Outline each uninfected red blood cell.
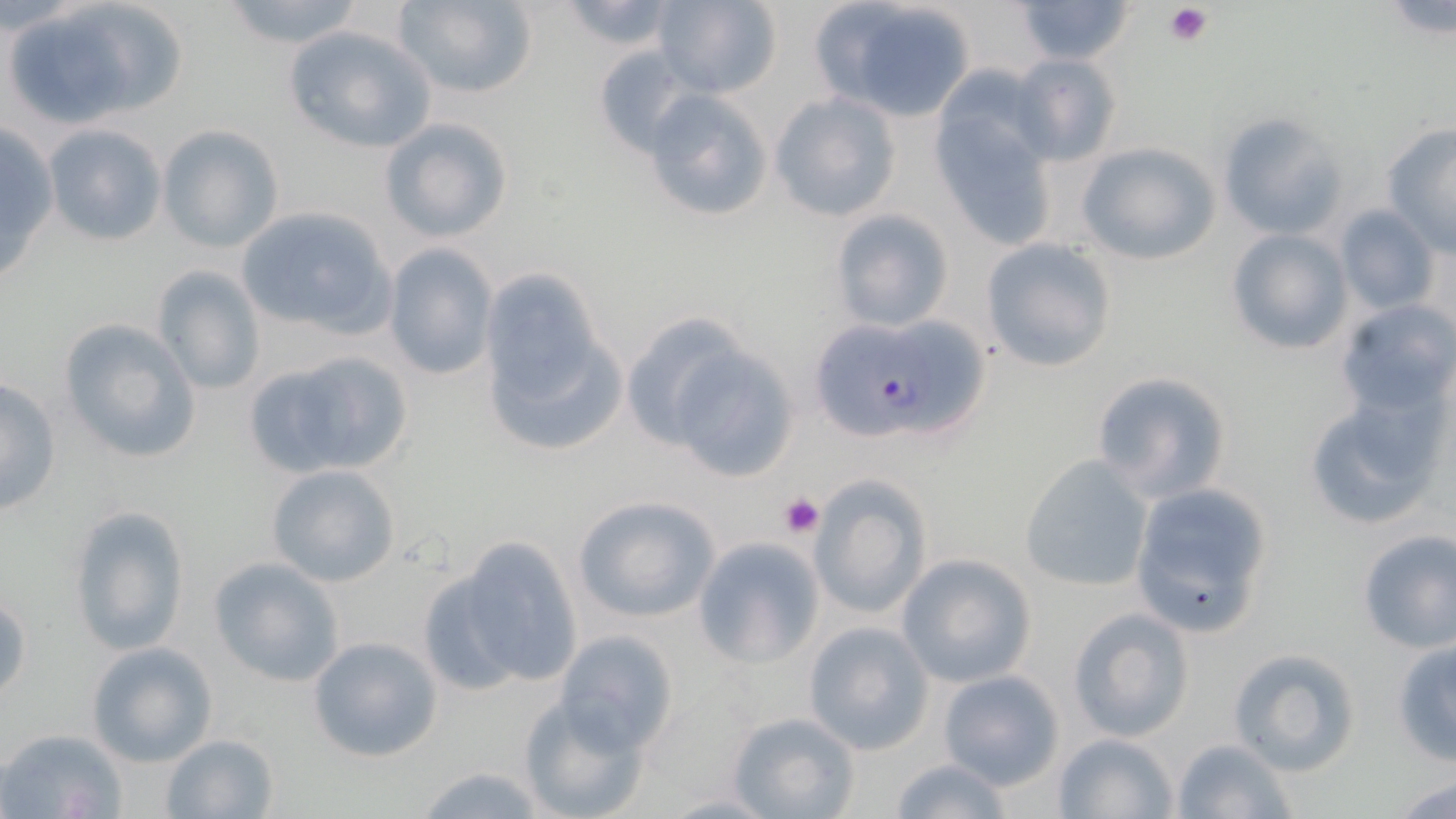

Approximate bounding boxes as named x1/y1/x2/y2 corners in pixels.
Uninfected red blood cells: (x1=12, y1=0, x2=186, y2=127), (x1=214, y1=0, x2=370, y2=49), (x1=393, y1=0, x2=538, y2=98), (x1=651, y1=0, x2=783, y2=97), (x1=809, y1=0, x2=981, y2=119), (x1=1016, y1=0, x2=1132, y2=64), (x1=556, y1=1, x2=682, y2=51), (x1=282, y1=23, x2=437, y2=154), (x1=591, y1=45, x2=699, y2=156), (x1=1011, y1=54, x2=1123, y2=167), (x1=642, y1=88, x2=774, y2=222), (x1=769, y1=91, x2=902, y2=222), (x1=931, y1=103, x2=1058, y2=252), (x1=1217, y1=112, x2=1349, y2=239), (x1=379, y1=115, x2=514, y2=243), (x1=0, y1=122, x2=58, y2=286), (x1=41, y1=124, x2=168, y2=247), (x1=156, y1=125, x2=284, y2=253), (x1=1380, y1=125, x2=1455, y2=252), (x1=1075, y1=140, x2=1220, y2=265), (x1=234, y1=205, x2=398, y2=342), (x1=1334, y1=206, x2=1440, y2=314), (x1=829, y1=208, x2=954, y2=332), (x1=1226, y1=229, x2=1352, y2=354), (x1=980, y1=237, x2=1118, y2=374), (x1=382, y1=243, x2=499, y2=381), (x1=153, y1=264, x2=267, y2=395), (x1=481, y1=276, x2=623, y2=455), (x1=1334, y1=300, x2=1456, y2=422), (x1=619, y1=310, x2=763, y2=455), (x1=59, y1=318, x2=201, y2=465), (x1=660, y1=340, x2=802, y2=483), (x1=244, y1=347, x2=414, y2=480), (x1=1090, y1=370, x2=1233, y2=503), (x1=1, y1=375, x2=63, y2=518), (x1=1303, y1=397, x2=1445, y2=530), (x1=1018, y1=453, x2=1153, y2=591), (x1=265, y1=464, x2=403, y2=588), (x1=803, y1=476, x2=932, y2=622), (x1=1128, y1=481, x2=1275, y2=639), (x1=571, y1=494, x2=721, y2=623), (x1=69, y1=503, x2=191, y2=659), (x1=1356, y1=529, x2=1456, y2=654), (x1=435, y1=534, x2=585, y2=695), (x1=692, y1=536, x2=825, y2=668), (x1=897, y1=554, x2=1036, y2=687), (x1=209, y1=556, x2=346, y2=687), (x1=1, y1=590, x2=31, y2=706), (x1=1066, y1=606, x2=1196, y2=741), (x1=802, y1=621, x2=934, y2=754), (x1=551, y1=629, x2=681, y2=754), (x1=306, y1=635, x2=444, y2=762), (x1=1390, y1=639, x2=1456, y2=768), (x1=85, y1=641, x2=218, y2=767), (x1=1227, y1=647, x2=1362, y2=775), (x1=936, y1=669, x2=1066, y2=790), (x1=518, y1=693, x2=651, y2=819), (x1=725, y1=710, x2=862, y2=819), (x1=2, y1=727, x2=128, y2=819), (x1=1051, y1=731, x2=1179, y2=818), (x1=159, y1=732, x2=280, y2=819), (x1=1168, y1=737, x2=1299, y2=819), (x1=886, y1=758, x2=1020, y2=819), (x1=410, y1=764, x2=554, y2=819), (x1=1389, y1=774, x2=1456, y2=817).

Platelet locations: (x1=1165, y1=4, x2=1212, y2=46), (x1=779, y1=493, x2=824, y2=537). Plasmodium falciparum-infected red blood cell locations: (x1=803, y1=316, x2=990, y2=450). Slide-level diagnosis: Plasmodium falciparum. Single field of view. Image is 1456×819 pixels. May-Grünwald-Giemsa stain. Optical microscopy. Thin blood smear. Captured at 1000x magnification.